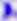

Toxoplasma gondii is shown. Captured at 400x magnification. Micrograph.